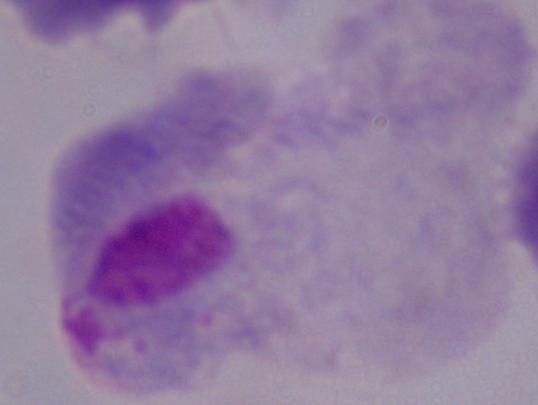

Summary:
  - Modality: photomicrograph
  - Identification: trichomonad
  - Magnification: 1000x